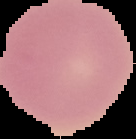
Summary:
  - Image type: segmented cell region with the area outside set to black
  - Result: negative for malaria parasites
  - Image size: 136×139 pixels
  - Preparation: thin blood film